Classify this cell by malaria status.
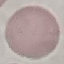
Uninfected.

Summary:
  - Image type: automatically extracted cell patch, resized to 64 × 64 pixels
  - Capture: smartphone through the microscope eyepiece
  - Stain: Giemsa
  - Preparation: thin blood film